Assess this cell for malaria.
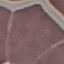

It is uninfected.

Summary:
  - Capture: smartphone through the microscope eyepiece
  - Preparation: thin blood film
  - Stain: Giemsa
  - Image type: automatically extracted cell patch, resized to 64 × 64 pixels